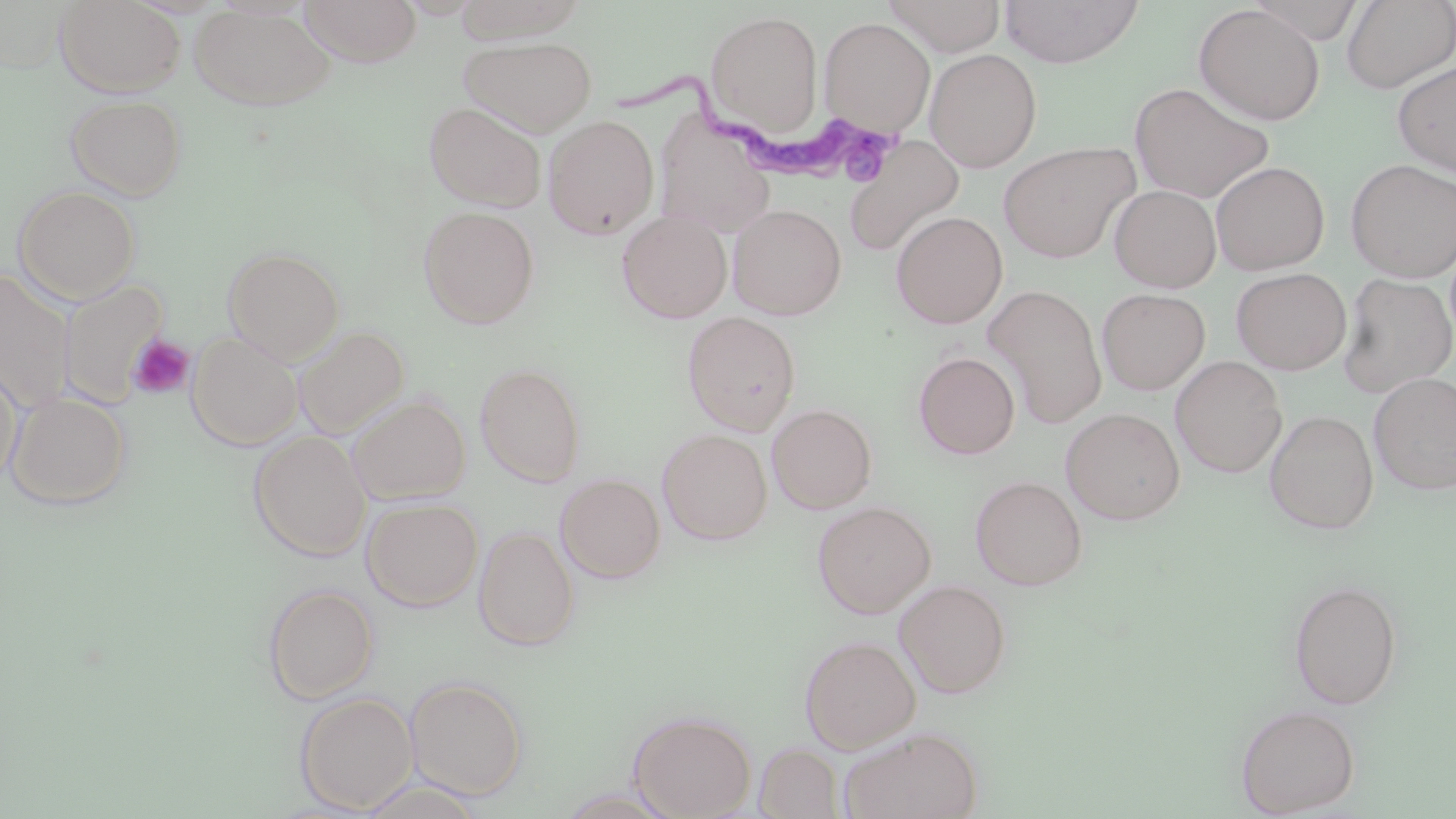

Approximate bounding boxes as (x1, y1, x2, y2) in pixels. Uninfected red blood cell locations: (54, 0, 186, 98), (299, 0, 420, 66), (452, 0, 588, 43), (882, 0, 1007, 56), (1000, 0, 1144, 68), (1247, 0, 1367, 43), (1341, 0, 1456, 94), (188, 5, 336, 111), (1193, 5, 1325, 125), (705, 10, 823, 136), (819, 17, 935, 135), (458, 36, 596, 137), (925, 48, 1042, 172), (1393, 61, 1456, 177), (1129, 82, 1274, 204), (64, 93, 188, 200), (423, 101, 547, 213), (543, 115, 659, 239), (844, 134, 965, 257), (998, 141, 1140, 263), (1346, 159, 1456, 282), (1212, 161, 1329, 274), (1109, 184, 1221, 292), (13, 185, 142, 303), (729, 204, 846, 320), (418, 206, 540, 329), (616, 210, 732, 323), (891, 211, 1008, 329), (222, 246, 345, 364), (1231, 267, 1351, 374), (0, 269, 76, 414), (1337, 273, 1456, 398), (58, 279, 168, 407), (984, 285, 1107, 428), (1097, 288, 1210, 395), (682, 312, 800, 434), (293, 325, 409, 440), (187, 331, 303, 450), (914, 352, 1020, 459), (1170, 355, 1287, 478), (0, 360, 23, 489), (475, 362, 587, 486), (1369, 372, 1456, 495), (5, 392, 132, 509), (347, 394, 471, 505), (767, 403, 877, 513), (1061, 408, 1185, 525), (1265, 409, 1379, 534), (658, 428, 772, 545), (249, 431, 371, 561), (555, 473, 666, 583), (971, 475, 1087, 590), (362, 497, 483, 611), (812, 501, 936, 618), (474, 526, 578, 651), (895, 579, 1011, 698), (1288, 579, 1402, 709), (262, 584, 379, 704), (799, 634, 921, 753), (405, 676, 528, 799), (294, 691, 418, 814), (1234, 704, 1360, 816), (628, 709, 756, 818), (840, 727, 981, 819), (755, 743, 843, 818), (356, 778, 485, 819), (556, 789, 679, 818). Platelet locations: (127, 334, 196, 400). Trypanosoma brucei locations: (622, 66, 898, 196). Slide-level diagnosis: Trypanosoma brucei. One field of a larger specimen. Thin blood smear. Captured at 1000x magnification. May-Grünwald-Giemsa-stained preparation. Light microscopy. Image is 1456×819 pixels.